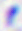

Summary:
  - Modality: micrograph
  - Magnification: 400x
  - Identification: Toxoplasma gondii